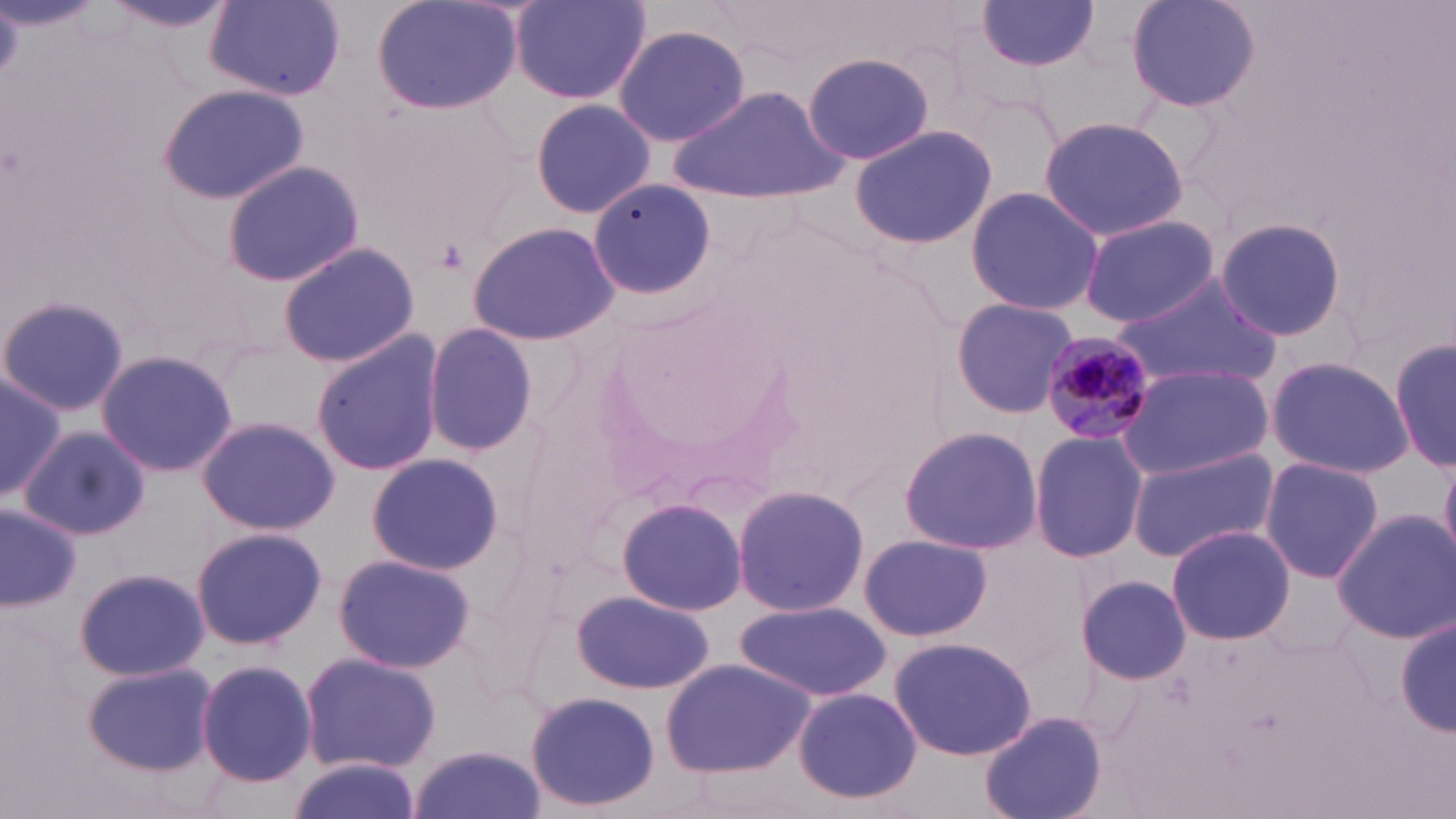
Approximate bounding boxes as (x1,y1)-(x2,y2) corner pairs in pixels. Plasmodium malariae-infected red blood cell locations: (1043,333)-(1150,442). Uninfected red blood cell locations: (372,0)-(522,113), (511,0)-(652,107), (1126,0)-(1262,112), (105,1)-(234,35), (205,2)-(346,99), (976,2)-(1103,77), (612,22)-(751,148), (803,50)-(935,166), (159,84)-(307,205), (675,86)-(843,203), (529,97)-(657,218), (1037,116)-(1192,242), (847,124)-(998,248), (222,161)-(365,287), (587,176)-(717,303), (964,186)-(1104,317), (1079,216)-(1222,327), (1216,217)-(1350,343), (468,220)-(622,347), (277,240)-(421,369), (1111,271)-(1284,392), (0,293)-(130,419), (950,297)-(1079,418), (421,321)-(540,457), (311,331)-(446,476), (1390,334)-(1456,472), (96,347)-(241,478), (1265,354)-(1413,479), (1117,364)-(1272,480), (0,372)-(66,505), (196,415)-(339,534), (897,423)-(1043,555), (21,427)-(151,541), (1029,428)-(1147,564), (1126,446)-(1279,563), (365,453)-(505,576), (1439,455)-(1456,560), (1258,457)-(1385,583), (731,484)-(871,617), (617,496)-(746,616), (0,505)-(83,611), (1331,510)-(1456,644), (1166,525)-(1295,645), (190,527)-(327,650), (859,533)-(992,641), (331,553)-(476,673), (73,566)-(210,683), (1075,574)-(1192,683), (573,588)-(716,696), (735,600)-(891,703), (1394,614)-(1454,740), (889,636)-(1038,761), (298,652)-(442,774), (196,658)-(318,788), (660,658)-(816,777), (82,660)-(218,776), (793,688)-(924,806), (526,690)-(661,814), (980,711)-(1107,819), (409,745)-(546,819), (284,758)-(422,819). Slide-level diagnosis: Plasmodium malariae. Light microscopy. Thin blood smear. May-Grünwald-Giemsa-stained preparation. 1000x magnification. Image is 1456×819 pixels. One field of a larger specimen.